Classify this cell by malaria status.
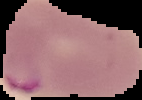

Parasitized.

Image is 142×100 pixels. From a thin blood film. Segmented cell region on a black background.